Give the preparation type.
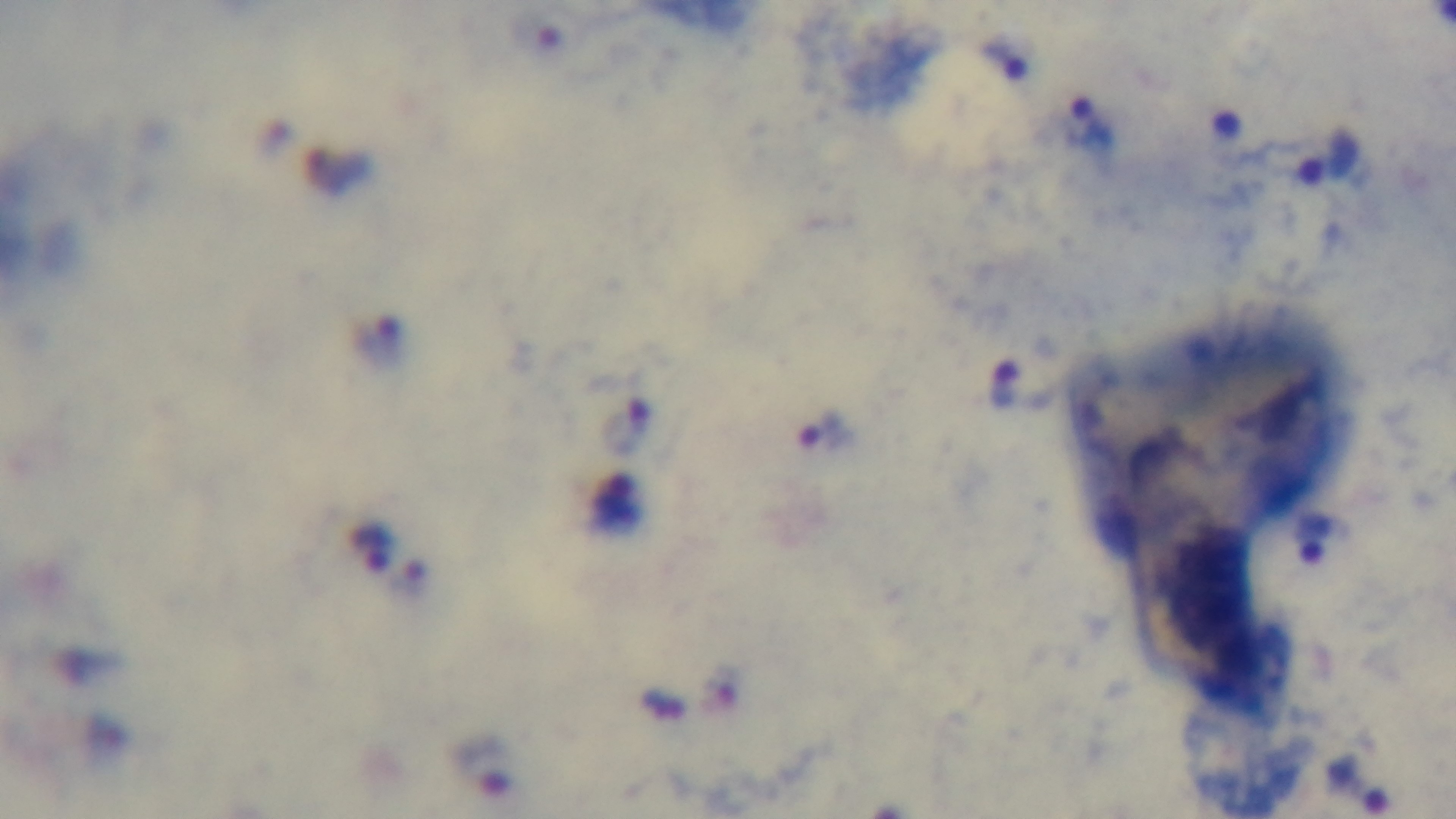

A thick smear.

Oil-immersion objective, 100x. Malaria status: positive. Photomicrograph. Mounted 4K digital camera. One field from the slide. Giemsa-stained.